Outline each uninfected red blood cell.
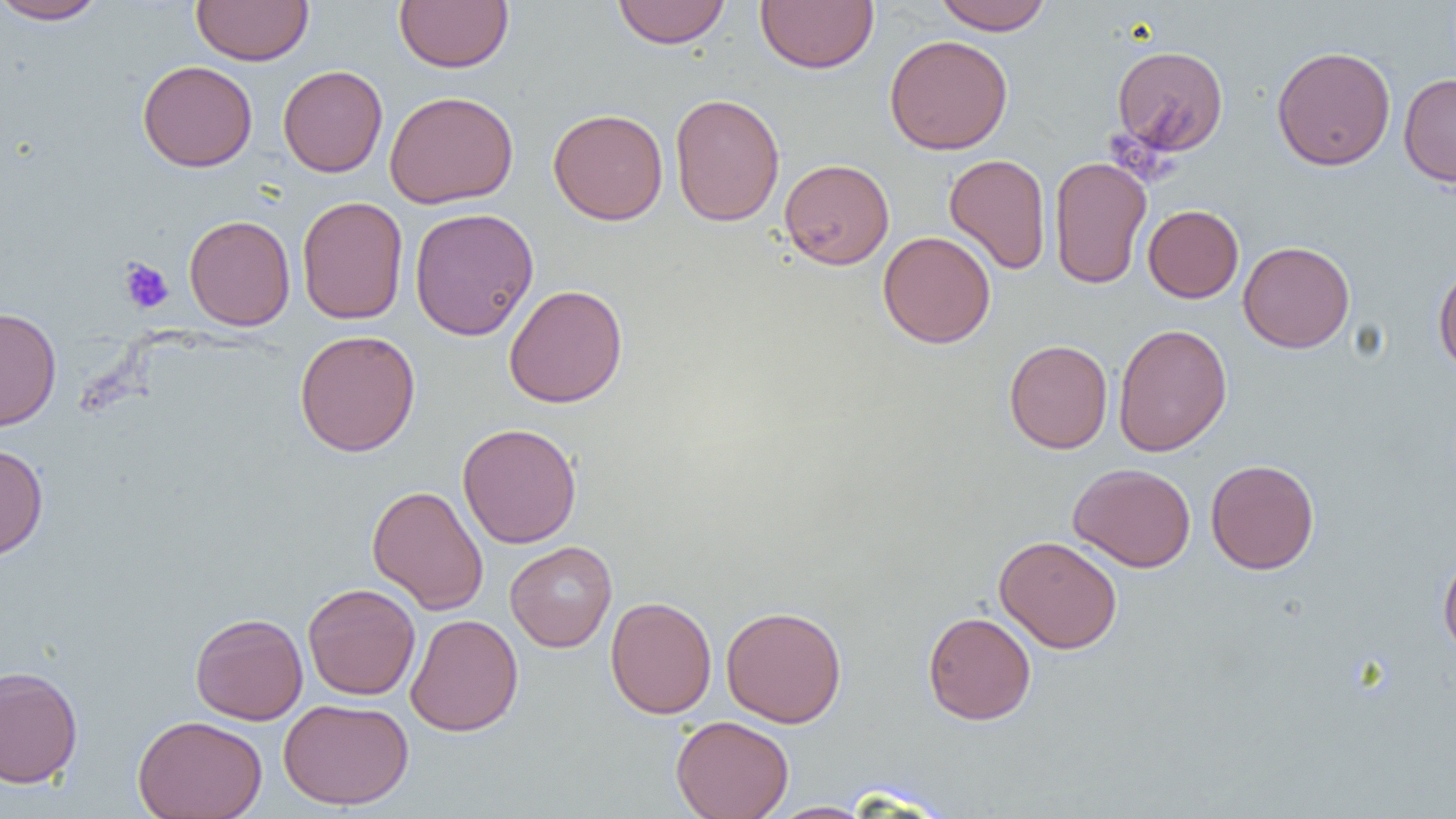

Approximate bounding boxes as [x1, y1, x2, y2] in pixels.
Uninfected red blood cells: [1, 0, 109, 25], [191, 0, 314, 66], [612, 0, 730, 48], [933, 0, 1053, 34], [395, 1, 513, 72], [756, 1, 878, 73], [884, 34, 1013, 155], [1112, 45, 1229, 157], [1272, 45, 1395, 171], [137, 60, 257, 172], [278, 65, 388, 177], [1398, 72, 1456, 188], [384, 90, 519, 209], [669, 93, 785, 226], [548, 108, 668, 225], [944, 154, 1051, 274], [1049, 155, 1152, 290], [779, 158, 894, 270], [296, 196, 409, 325], [1143, 205, 1244, 303], [409, 207, 539, 341], [184, 214, 296, 331], [878, 231, 995, 348], [1238, 241, 1355, 353], [1433, 263, 1456, 377], [504, 284, 628, 408], [0, 307, 62, 431], [1113, 323, 1232, 457], [294, 329, 421, 456], [1004, 339, 1113, 454], [457, 422, 582, 548], [0, 443, 49, 561], [1206, 459, 1320, 575], [1068, 462, 1196, 572], [367, 484, 488, 615], [993, 535, 1123, 654], [505, 541, 617, 652], [1438, 549, 1456, 660], [302, 583, 420, 700], [605, 596, 717, 718], [721, 605, 847, 727], [922, 611, 1036, 725], [190, 613, 308, 725], [406, 614, 523, 736], [0, 665, 84, 789], [278, 698, 414, 810], [133, 715, 267, 819], [671, 715, 794, 819], [766, 801, 876, 818].

Summary:
  - Platelet locations: [119, 258, 174, 314]
  - Slide-level diagnosis: no evidence of blood parasites
  - Image size: 1456×819 pixels
  - Modality: optical microscopy
  - Preparation: thin blood smear
  - Field of view: single
  - Magnification: 1000x